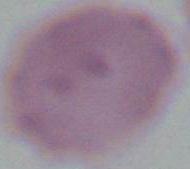

identification: erythrocyte
modality: photomicrograph
magnification: 1000x